Comment on the morphology of the erythrocytes.
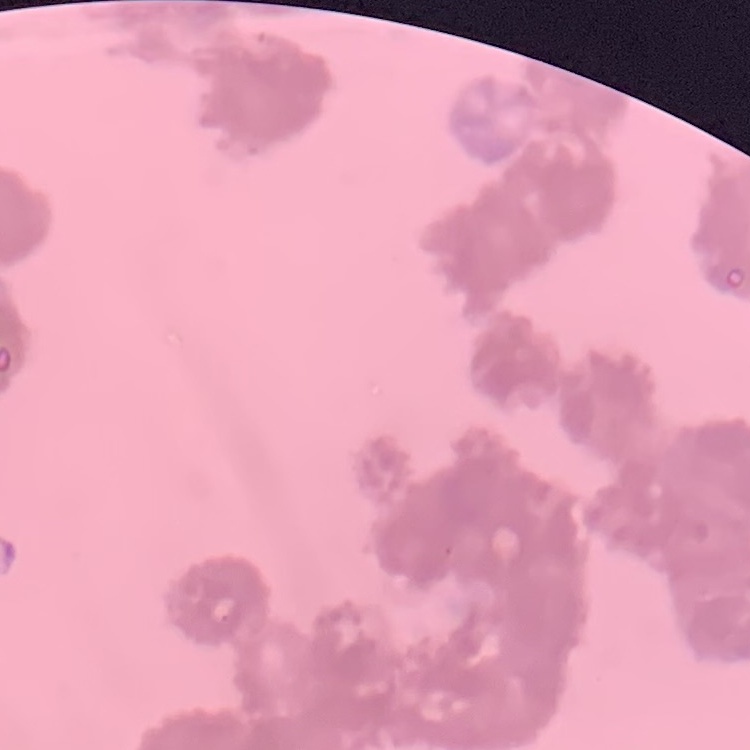

Rouleaux formation.

image_type: one tile cut from a larger photomicrograph
stain: Field's or Giemsa
preparation: thin blood film